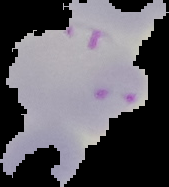
Summary:
  - Image size: 169×187 pixels
  - Malaria status: parasitized
  - Image type: segmented cell region with the area outside set to black
  - Preparation: thin blood film